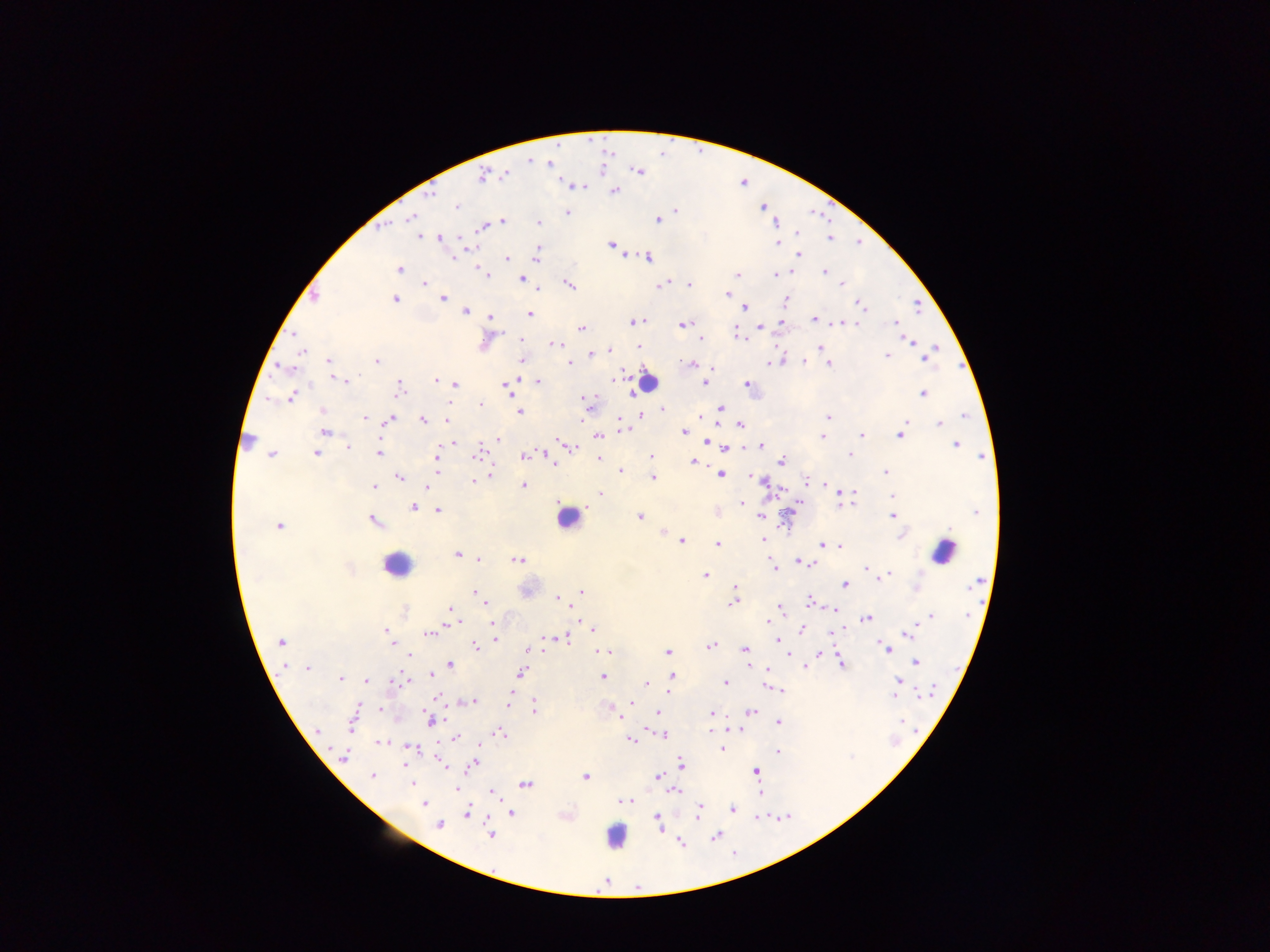
country = Ghana
image size = 1270×952 pixels
Plasmodium parasite locations = approximate centers as {x, y} in pixels: {529, 160}, {551, 163}, {636, 170}, {504, 174}, {482, 175}, {575, 186}, {614, 192}, {430, 195}, {456, 206}, {676, 210}, {567, 212}, {412, 217}, {657, 219}, {503, 220}, {537, 223}, {484, 226}, {796, 234}, {418, 235}, {440, 238}, {829, 238}, {778, 242}, {613, 244}, {463, 247}, {536, 254}, {796, 255}, {625, 256}, {648, 256}, {454, 257}, {505, 258}, {399, 269}, {481, 269}, {824, 271}, {789, 273}, {485, 274}, {737, 274}, {774, 274}, {521, 279}, {424, 283}, {842, 283}, {568, 284}, {663, 284}, {688, 284}, {536, 289}, {727, 295}, {315, 296}, {442, 298}, {394, 299}, {785, 301}, {859, 302}, {744, 307}, {464, 311}, {527, 313}, {490, 318}, {814, 319}, {783, 320}, {641, 321}, {633, 322}, {780, 322}, {837, 323}, {853, 323}, {895, 323}, {681, 325}, {580, 328}, {759, 328}, {735, 333}, {520, 338}, {700, 338}, {911, 341}, {554, 345}, {638, 347}, {820, 347}, {936, 347}, {609, 350}, {301, 351}, {593, 352}, {887, 356}, {925, 358}, {375, 361}, {521, 361}, {780, 361}, {804, 361}, {328, 362}, {568, 363}, {767, 363}, {828, 363}, {693, 364}, {285, 367}, {331, 376}, {617, 377}, {338, 378}, {343, 381}, {436, 381}, {537, 382}, {705, 382}, {454, 384}, {747, 384}, {504, 385}, {398, 388}, {629, 393}, {922, 393}, {291, 396}, {584, 399}, {269, 400}, {450, 401}, {479, 403}, {662, 408}, {717, 410}, {321, 411}, {519, 411}, {640, 416}, {828, 416}, {963, 416}, {365, 418}, {583, 418}, {388, 419}, {423, 420}, {447, 420}, {618, 420}, {938, 424}, {740, 425}, {620, 429}, {325, 431}, {684, 432}, {900, 433}, {597, 435}, {861, 435}, {822, 436}, {495, 438}, {558, 440}, {455, 441}, {707, 442}, {563, 443}, {955, 444}, {347, 447}, {571, 447}, {725, 447}, {760, 447}, {316, 453}, {379, 453}, {271, 454}, {477, 454}, {849, 454}, {523, 455}, {547, 456}, {436, 457}, {651, 457}, {598, 458}, {694, 461}, {780, 462}, {553, 464}, {437, 471}, {620, 471}, {884, 471}, {489, 473}, {720, 474}, {750, 476}, {399, 477}, {653, 478}, {472, 480}, {762, 481}, {806, 481}, {524, 485}, {373, 486}, {426, 489}, {782, 491}, {601, 494}, {837, 494}, {893, 495}, {852, 500}, {740, 502}, {799, 503}, {795, 505}, {413, 508}, {438, 510}, {717, 512}, {892, 515}, {760, 516}, {639, 517}, {373, 521}, {784, 523}, {279, 525}, {663, 531}, {900, 535}, {681, 540}, {764, 540}, {717, 543}, {822, 545}, {838, 545}, {457, 554}, {479, 560}, {518, 560}, {798, 561}, {805, 562}, {772, 565}, {812, 565}, {866, 568}, {705, 575}, {884, 577}, {844, 584}, {734, 587}, {916, 589}, {582, 591}, {473, 592}, {558, 598}, {733, 601}, {808, 603}, {486, 605}, {779, 607}, {450, 608}, {571, 609}, {835, 609}, {930, 616}, {452, 617}, {866, 618}, {455, 621}, {491, 622}, {767, 623}, {590, 628}, {842, 628}, {800, 629}, {385, 630}, {428, 633}, {909, 633}, {547, 637}, {566, 637}, {495, 639}, {776, 640}, {281, 642}, {710, 645}, {392, 646}, {475, 646}, {744, 648}, {885, 649}, {528, 650}, {606, 651}, {667, 653}, {820, 653}, {789, 655}, {408, 656}, {840, 661}, {915, 662}, {450, 665}, {804, 666}, {307, 668}, {765, 669}, {521, 673}, {431, 674}, {671, 676}, {340, 677}, {603, 677}, {366, 680}, {899, 680}, {669, 682}, {725, 682}, {646, 685}, {767, 687}, {776, 689}, {780, 690}, {438, 695}, {510, 695}, {893, 695}, {472, 701}, {507, 701}, {630, 702}, {534, 707}, {379, 709}, {610, 710}, {750, 711}, {657, 712}, {711, 713}, {621, 715}, {430, 720}, {902, 720}, {353, 721}, {778, 722}, {647, 727}, {730, 728}, {317, 731}, {711, 732}, {500, 733}, {664, 734}, {456, 738}, {631, 739}, {381, 742}, {409, 746}, {722, 749}, {776, 752}, {343, 758}, {472, 763}, {680, 763}, {445, 764}, {756, 771}, {372, 776}, {585, 776}, {657, 776}, {412, 783}, {525, 784}, {456, 788}, {490, 791}, {674, 791}, {759, 793}, {494, 794}, {627, 801}, {422, 803}, {699, 806}, {732, 809}, {467, 812}, {511, 813}, {697, 813}, {657, 816}, {758, 816}, {659, 823}, {439, 825}, {491, 834}, {715, 836}, {680, 842}
preparation = thick blood film
capture = mobile-phone photograph through a microscope
leukocyte locations = approximate centers as {x, y} in pixels: {645, 381}, {249, 440}, {568, 518}, {944, 551}, {396, 564}, {616, 836}
field of view = single